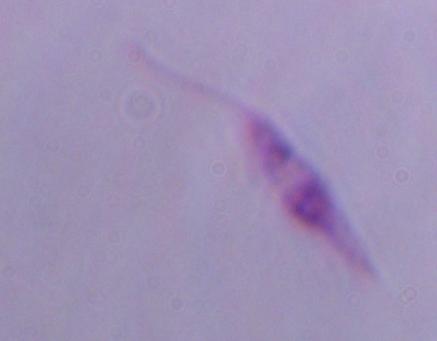 Micrograph. 1000x magnification. A Leishmania parasite is shown.